State which cell type is depicted.
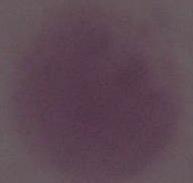

This is an erythrocyte.

Summary:
  - Magnification: 1000x
  - Modality: micrograph